Classify the preparation.
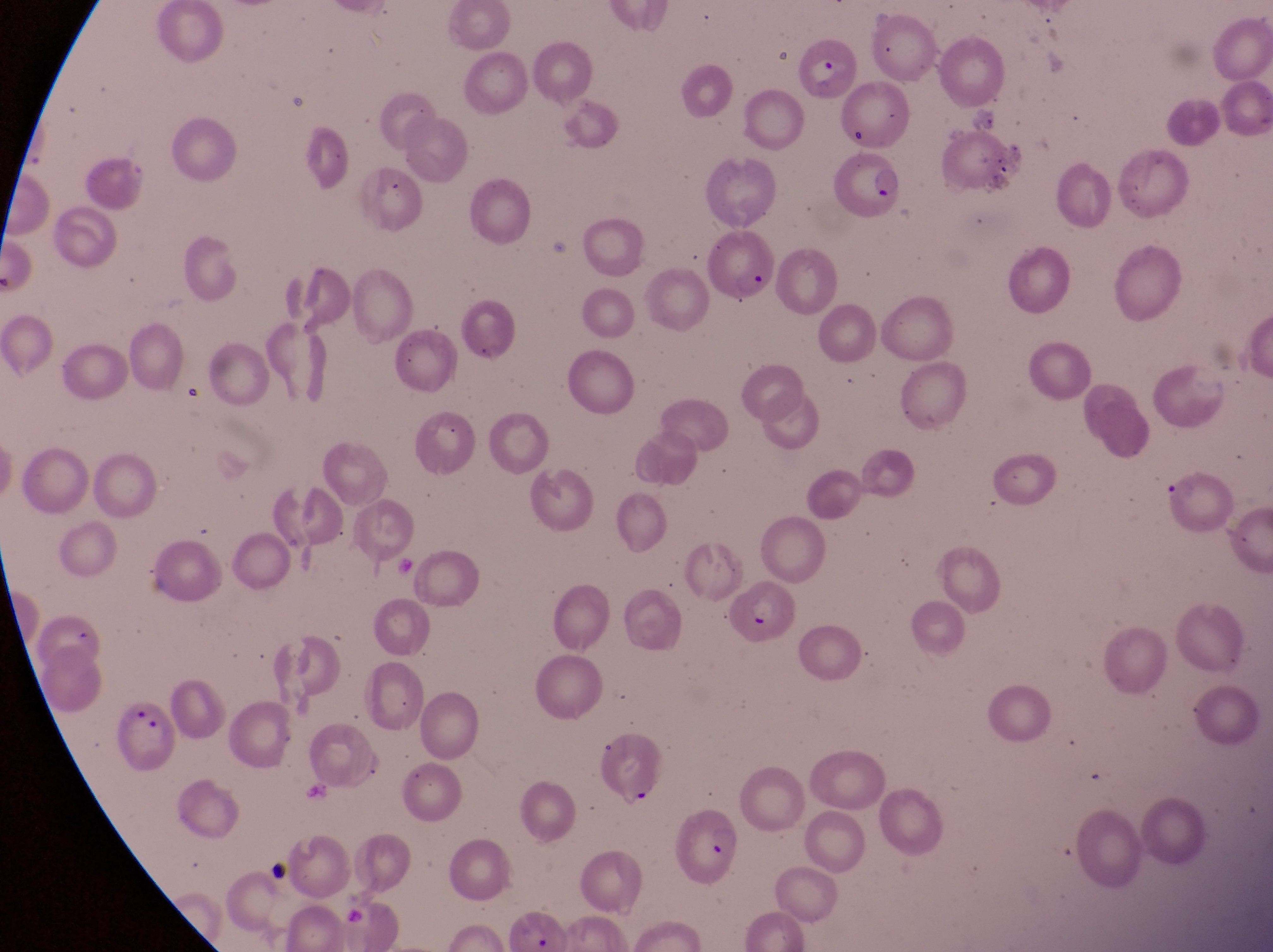
This is a thin smear.

Approximate bounding boxes as left top right bottom in pixels. Artifact (platelet-like body, stain precipitate, or debris) locations: 968 98 1001 133. Parasitised red blood cell locations: 792 33 857 100; 833 152 907 220; 708 227 780 310; 726 584 800 639; 113 694 176 771; 596 722 665 807; 671 802 743 890. Single field of view. Image is 1273×952 pixels. At a magnification of 1000x. Collected in Uganda. Photographed through the eyepiece of an Olympus CX-23 microscope with a smartphone camera.